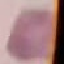

result = no malaria parasites detected
image type = cell patch, automatically extracted from a larger field of view and resized to 64 × 64 pixels
preparation = thin blood smear
capture = smartphone camera at the microscope eyepiece
stain = Giemsa